Comment on the morphology of the red blood cells.
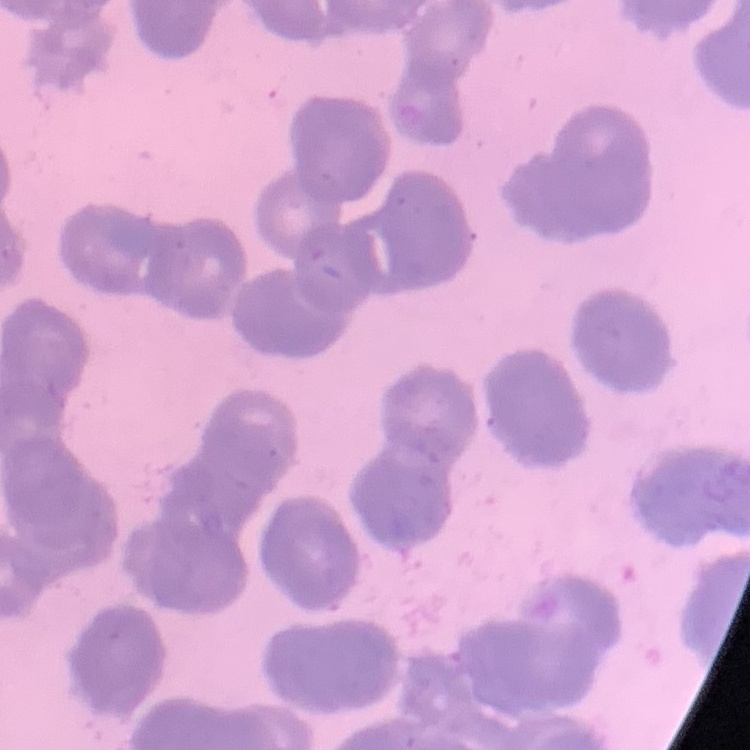

They show rouleaux formation.

Summary:
  - Image type: square crop of a larger photomicrograph
  - Stain: Field's or Giemsa
  - Preparation: thin blood smear